Classify this cell by malaria status.
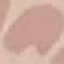
Uninfected.

preparation = thin blood smear
capture = smartphone camera at the microscope eyepiece
image type = cell patch, automatically extracted from a larger field of view and resized to 64 × 64 pixels
stain = Giemsa